Name the blood parasite species.
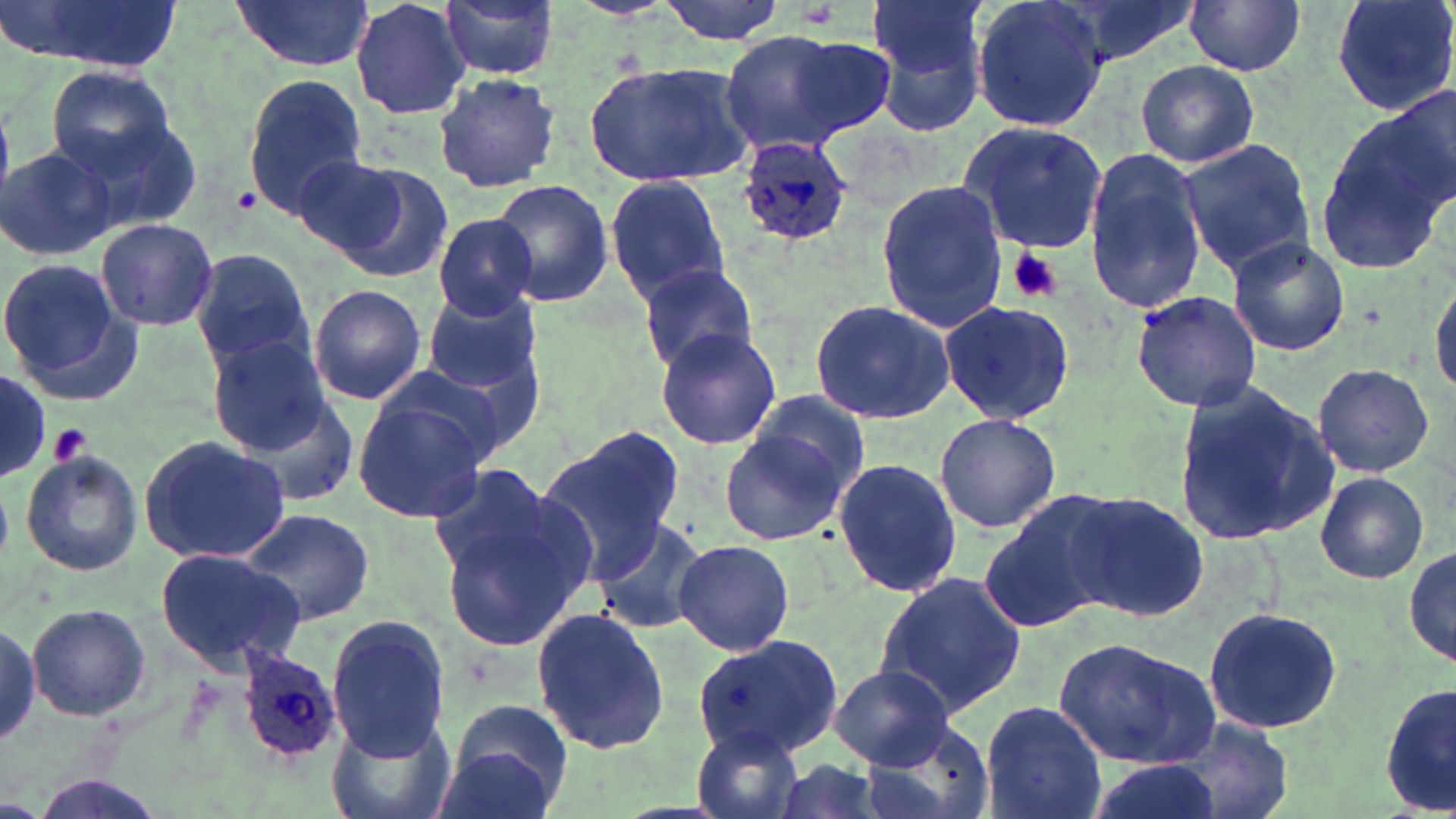

Plasmodium ovale.

Summary:
  - Coordinate format: approximate bounding boxes as [x1, y1, x2, y2] in pixels
  - Plasmodium ovale-infected red blood cell locations: [735, 136, 853, 247], [234, 646, 341, 765]
  - Uninfected red blood cell locations: [10, 0, 184, 70], [228, 0, 375, 72], [350, 0, 472, 120], [440, 0, 558, 80], [654, 0, 788, 44], [867, 0, 986, 83], [970, 0, 1109, 135], [1049, 0, 1201, 65], [1183, 0, 1307, 76], [1330, 0, 1456, 120], [874, 28, 988, 138], [719, 31, 861, 154], [785, 35, 898, 137], [585, 57, 754, 187], [1135, 59, 1258, 168], [45, 68, 182, 183], [431, 71, 561, 195], [242, 74, 368, 219], [1367, 89, 1456, 221], [1314, 97, 1456, 271], [63, 113, 204, 238], [957, 120, 1110, 253], [1178, 138, 1317, 276], [0, 145, 118, 259], [1081, 148, 1208, 317], [300, 155, 448, 278], [603, 175, 732, 303], [487, 179, 614, 307], [875, 181, 1008, 330], [428, 213, 542, 318], [95, 218, 218, 331], [1225, 236, 1351, 357], [191, 248, 315, 373], [0, 258, 133, 394], [634, 261, 761, 374], [1428, 277, 1456, 400], [309, 285, 427, 404], [1131, 289, 1262, 412], [423, 291, 542, 394], [808, 298, 955, 425], [938, 299, 1075, 427], [653, 324, 783, 451], [205, 333, 334, 454], [1313, 362, 1435, 478], [371, 363, 522, 470], [0, 373, 51, 478], [1172, 378, 1339, 546], [235, 389, 363, 504], [743, 392, 872, 512], [352, 397, 486, 524], [934, 413, 1061, 535], [719, 423, 851, 547], [537, 432, 681, 576], [136, 435, 291, 567], [19, 451, 142, 576], [833, 457, 960, 600], [424, 463, 558, 580], [1315, 472, 1431, 584], [437, 489, 598, 655], [1063, 489, 1210, 623], [981, 495, 1123, 633], [240, 506, 375, 626], [590, 514, 712, 637], [1404, 538, 1455, 675], [672, 539, 795, 657], [153, 548, 308, 673], [873, 571, 1027, 720], [27, 605, 150, 721], [1201, 606, 1344, 733], [533, 608, 671, 755], [327, 616, 449, 760], [0, 622, 39, 748], [695, 632, 847, 762], [1054, 636, 1221, 767], [829, 665, 953, 768], [1381, 681, 1455, 819], [443, 696, 579, 813], [979, 700, 1107, 819], [324, 709, 459, 819], [1167, 716, 1295, 819], [861, 720, 996, 819], [691, 727, 808, 819], [1082, 756, 1225, 819], [770, 758, 890, 819]
  - Platelet locations: [231, 185, 264, 215], [1007, 248, 1064, 305], [50, 422, 92, 468]
  - Preparation: thin blood film
  - Stain: May-Grünwald-Giemsa
  - Modality: optical microscopy
  - Image size: 1456×819 pixels
  - Field of view: single
  - Magnification: 1000x